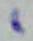

Captured at 1000x magnification. Toxoplasma gondii is shown. Photomicrograph.